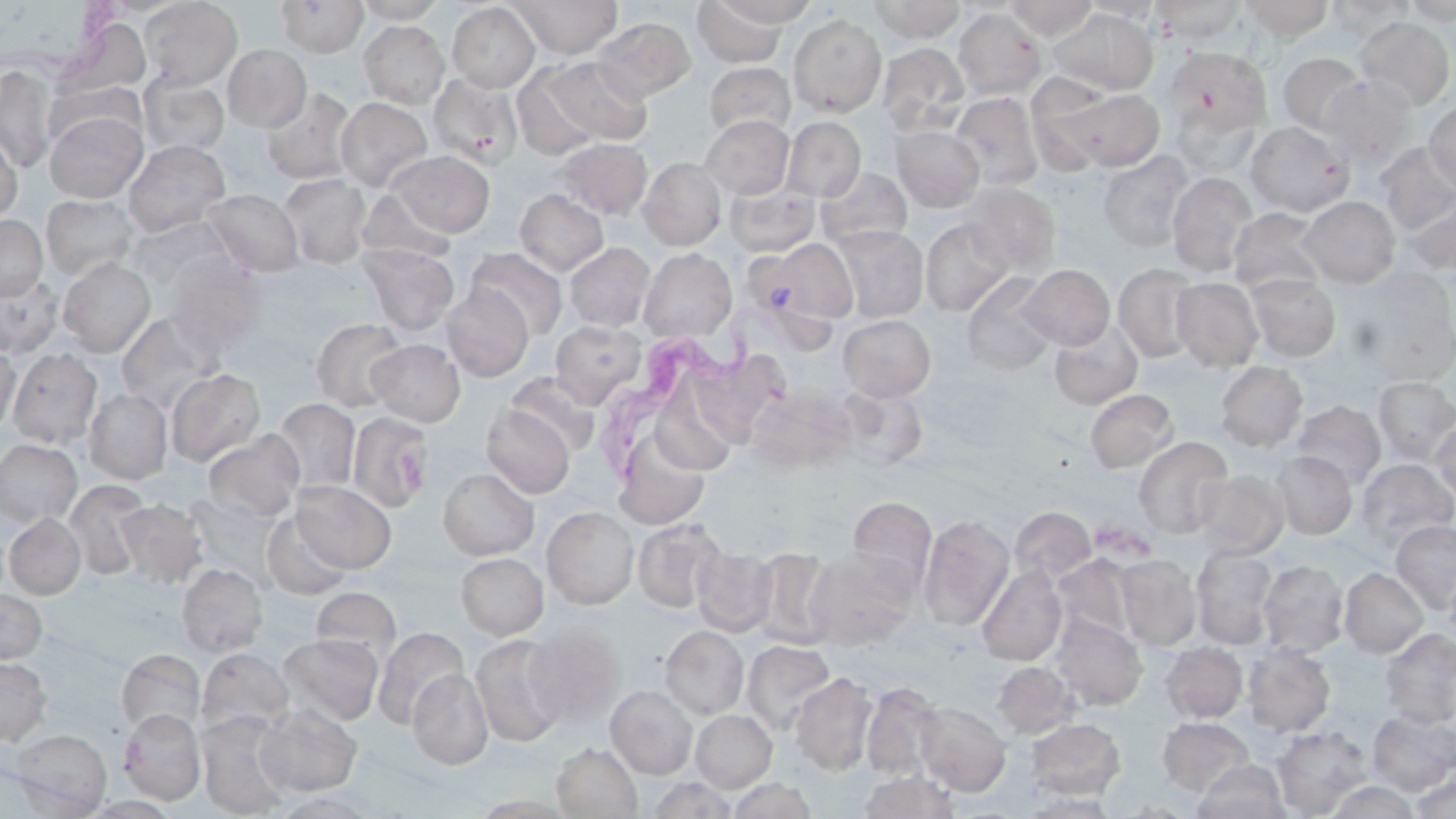
Trypanosoma brucei locations = approximate bounding boxes as [x1, y1, x2, y2] in pixels: [602, 316, 759, 485]
slide-level diagnosis = Trypanosoma brucei
modality = optical microscopy
preparation = thin blood smear
image size = 1456×819 pixels
magnification = 1000x
uninfected red blood cell locations = approximate bounding boxes as [x1, y1, x2, y2] in pixels: [276, 0, 367, 57], [353, 0, 448, 23], [510, 0, 622, 58], [713, 0, 819, 26], [1003, 0, 1099, 40], [1240, 0, 1333, 41], [1326, 0, 1415, 43], [1401, 0, 1456, 25], [140, 1, 242, 89], [692, 1, 789, 68], [868, 1, 966, 43], [1081, 1, 1164, 20], [1149, 1, 1247, 44], [447, 3, 540, 92], [953, 7, 1046, 101], [1047, 8, 1159, 95], [788, 14, 887, 117], [56, 15, 153, 100], [593, 17, 696, 101], [1354, 17, 1455, 111], [358, 21, 449, 109], [876, 42, 970, 136], [223, 44, 311, 132], [1162, 45, 1273, 142], [1277, 52, 1367, 136], [544, 56, 652, 146], [703, 61, 795, 140], [513, 64, 600, 160], [0, 65, 58, 174], [427, 73, 523, 170], [139, 74, 230, 157], [1318, 75, 1417, 169], [45, 82, 143, 149], [261, 87, 357, 184], [1060, 87, 1166, 172], [949, 91, 1044, 191], [336, 96, 433, 192], [1423, 100, 1456, 193], [44, 110, 147, 203], [700, 115, 794, 198], [781, 116, 866, 202], [1245, 121, 1351, 216], [892, 126, 985, 212], [0, 131, 22, 226], [556, 138, 652, 219], [123, 139, 231, 237], [1376, 143, 1456, 234], [1097, 150, 1195, 251], [390, 151, 494, 237], [638, 156, 727, 251], [816, 167, 912, 249], [1167, 172, 1257, 277], [277, 173, 372, 268], [724, 179, 821, 257], [960, 183, 1060, 274], [358, 188, 457, 264], [202, 189, 304, 276], [515, 189, 609, 276], [1402, 193, 1456, 276], [41, 194, 139, 280], [1299, 195, 1400, 288], [1229, 207, 1327, 295], [0, 215, 47, 301], [126, 216, 237, 289], [920, 218, 1015, 316], [830, 225, 928, 322], [748, 238, 858, 332], [564, 242, 655, 332], [358, 244, 460, 336], [465, 247, 568, 339], [639, 248, 736, 342], [165, 254, 266, 354], [58, 258, 155, 357], [1019, 264, 1114, 350], [1113, 264, 1202, 361], [0, 273, 63, 356], [1245, 273, 1341, 362], [962, 274, 1058, 375], [1171, 277, 1264, 370], [441, 285, 534, 382], [115, 312, 223, 414], [838, 315, 936, 401], [311, 318, 408, 412], [551, 320, 646, 408], [1049, 322, 1143, 410], [366, 338, 465, 426], [0, 343, 20, 438], [687, 348, 788, 446], [7, 349, 103, 449], [1214, 361, 1307, 451], [166, 368, 265, 467], [505, 375, 601, 457], [1373, 376, 1456, 465], [640, 377, 745, 479], [745, 383, 855, 472], [832, 384, 929, 472], [85, 388, 173, 484], [1085, 388, 1178, 472], [273, 398, 360, 494], [1291, 401, 1386, 488], [481, 403, 575, 498], [346, 411, 434, 516], [1431, 418, 1456, 500], [611, 425, 712, 529], [203, 429, 305, 522], [1133, 436, 1233, 538], [0, 439, 82, 527], [1273, 451, 1357, 540], [1355, 458, 1455, 553], [438, 468, 538, 560], [1194, 469, 1289, 557], [64, 480, 150, 580], [291, 480, 397, 573], [847, 496, 937, 595], [116, 499, 207, 587], [542, 506, 639, 609], [1010, 507, 1097, 585], [260, 509, 352, 600], [4, 513, 86, 599], [918, 514, 1015, 630], [632, 518, 728, 613], [1391, 520, 1456, 613], [691, 545, 777, 636], [1191, 546, 1278, 649], [752, 547, 840, 648], [803, 550, 915, 649], [456, 552, 548, 640], [1116, 555, 1201, 651], [1054, 556, 1135, 640], [1258, 560, 1348, 657], [177, 563, 268, 658], [977, 565, 1068, 666], [1339, 567, 1428, 658], [310, 586, 402, 666], [0, 590, 46, 663], [1049, 613, 1148, 711], [660, 626, 749, 718], [372, 627, 468, 730], [524, 627, 625, 725], [1379, 628, 1456, 727], [277, 633, 384, 726], [470, 634, 568, 748], [742, 640, 838, 735], [1162, 642, 1248, 723], [1242, 643, 1335, 737], [116, 648, 205, 735], [196, 648, 295, 738], [0, 658, 52, 745], [991, 661, 1079, 739], [408, 668, 493, 770], [789, 672, 879, 776], [860, 682, 944, 780], [606, 685, 697, 779], [914, 701, 1011, 795], [255, 703, 362, 796], [119, 708, 206, 804], [1365, 709, 1456, 796], [691, 710, 776, 792], [197, 712, 293, 818], [1158, 717, 1255, 795], [1024, 718, 1126, 800], [1271, 726, 1372, 817], [8, 728, 112, 817], [551, 742, 643, 818], [1193, 760, 1290, 818], [857, 770, 961, 819], [1410, 773, 1456, 818], [648, 776, 737, 818], [728, 777, 817, 819], [1325, 781, 1421, 818], [266, 791, 383, 818], [81, 796, 181, 818]
platelet locations = approximate bounding boxes as [x1, y1, x2, y2] in pixels: [398, 455, 430, 494]
field of view = one of a larger specimen
stain = May-Grünwald-Giemsa